Give the position of every leukocyte visible.
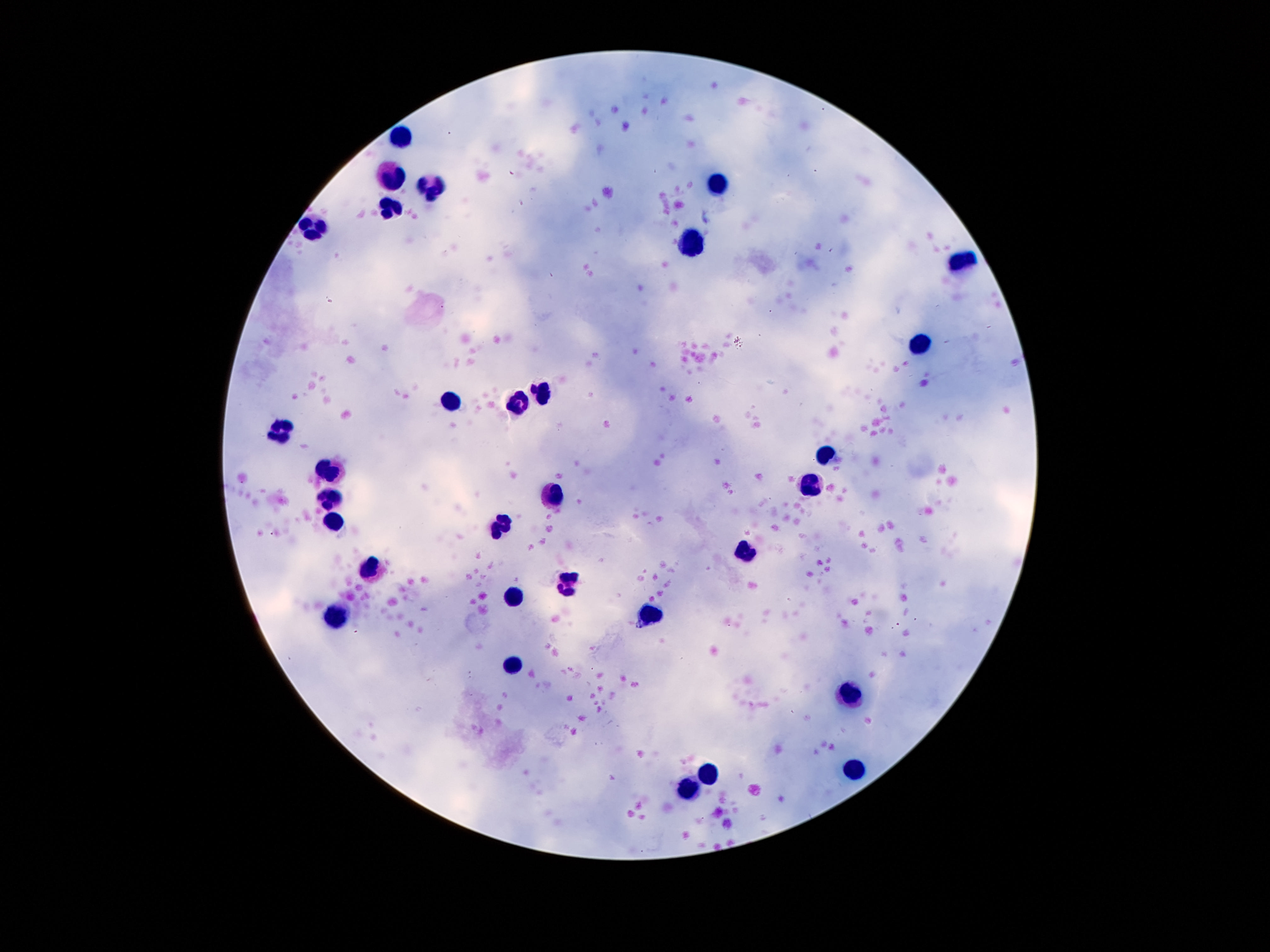

Approximate object centers, in pixels from the top-left corner.
Leukocytes: (x=401, y=138), (x=392, y=173), (x=718, y=184), (x=437, y=186), (x=388, y=211), (x=311, y=228), (x=693, y=242), (x=961, y=259), (x=917, y=346), (x=541, y=391), (x=449, y=400), (x=516, y=402), (x=285, y=429), (x=829, y=454), (x=329, y=472), (x=814, y=484), (x=554, y=492), (x=330, y=497), (x=334, y=521), (x=500, y=524), (x=745, y=550), (x=371, y=566), (x=565, y=583), (x=516, y=597), (x=336, y=617), (x=651, y=617), (x=512, y=667), (x=846, y=692), (x=710, y=770), (x=852, y=771), (x=688, y=791).

Summary:
  - Capture: smartphone camera through the microscope eyepiece
  - Image size: 1270×952 pixels
  - Field of view: one from this slide
  - Magnification: 100x
  - Stain: Giemsa
  - Preparation: thick peripheral-blood smear
  - Patient malaria status: negative